Outline each P. falciparum parasite and classify it by life-cycle stage.
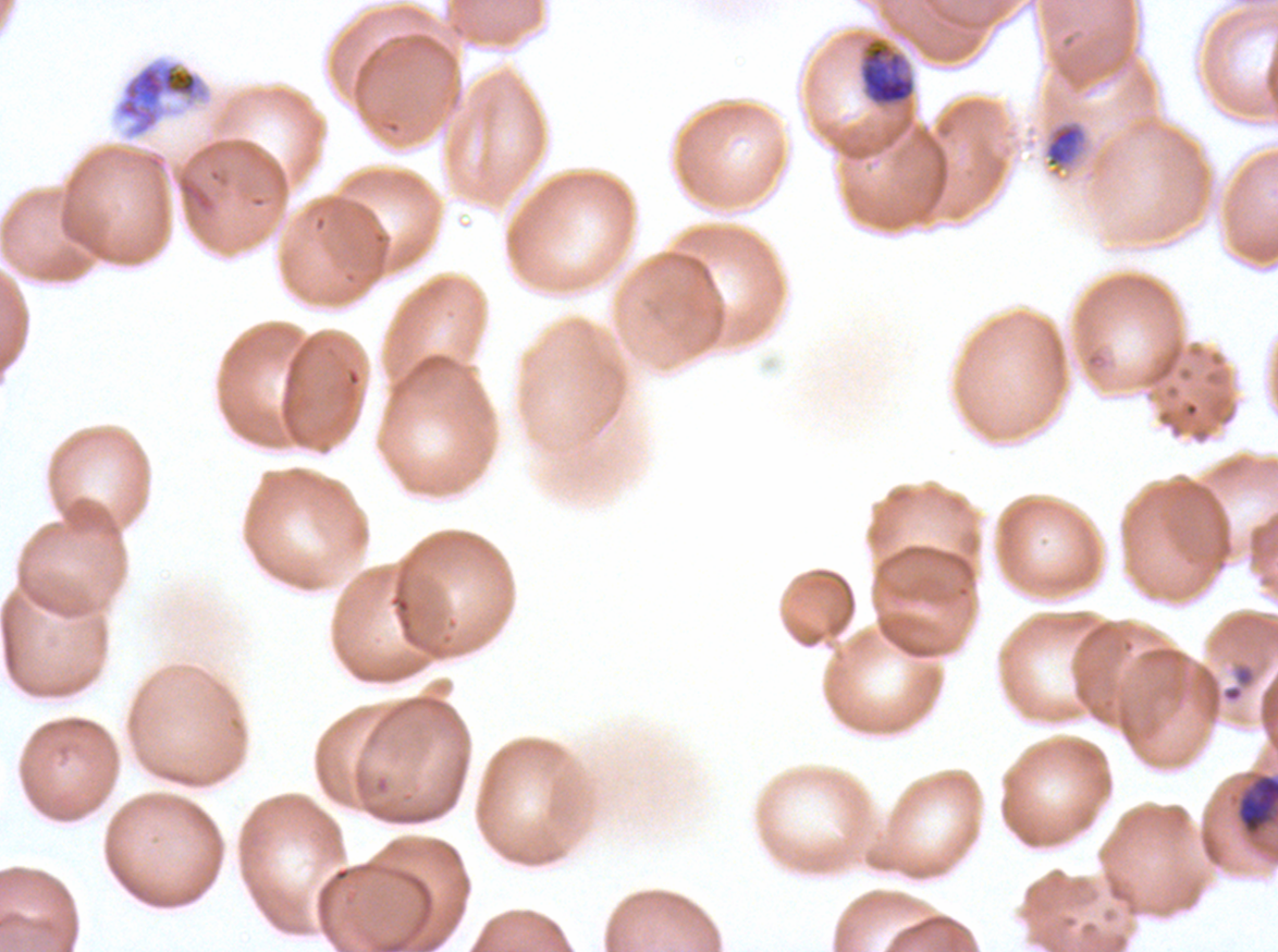

Approximate bounding rectangles given as corner coordinates in pixels from the top-left.
Late-ring/early-trophozoite forms: (x1=1222, y1=664, x2=1256, y2=703).
Late trophozoites: (x1=860, y1=39, x2=915, y2=106), (x1=1040, y1=116, x2=1095, y2=183), (x1=1237, y1=775, x2=1277, y2=833).
Early schizonts: (x1=112, y1=55, x2=214, y2=141).
No rings, mid trophozoites, late schizonts, segmenters, or gametocytes observed.

field of view = one sub-image of a larger composite
preparation = thin blood smear
specimen = P. falciparum cultured ex vivo for 24 to 48 hours, from a patient in The Gambia
image size = 1278×952 pixels
life-cycle stages observed = late-ring/early-trophozoite, late trophozoite, early schizont
stain = Giemsa